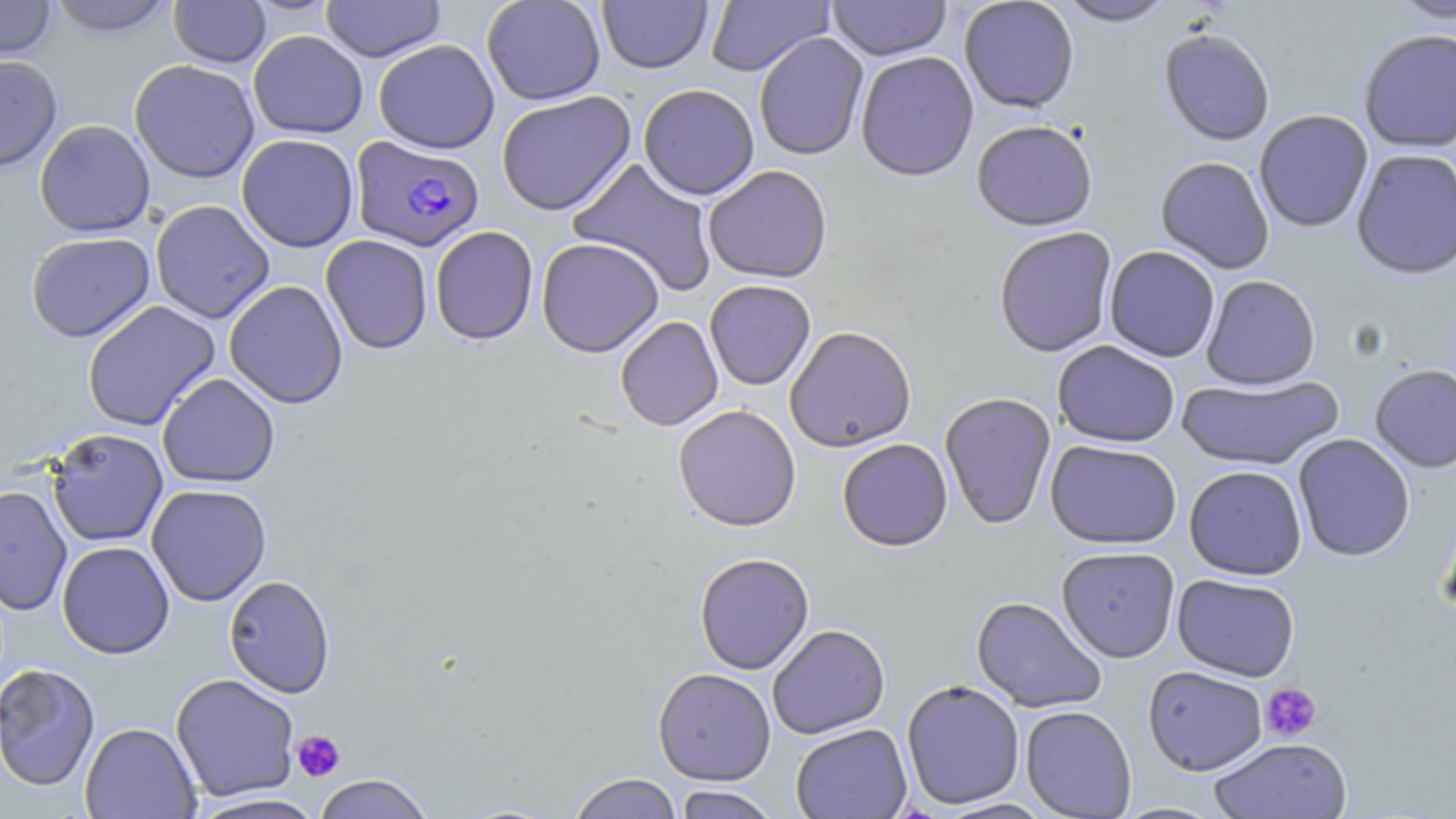
plasmodium_falciparum_infected_red_blood_cell_locations: 'approximate bounding boxes as named x1/y1/x2/y2 corners in pixels: (x1=350, y1=136, x2=485, y2=252)'
slide_level_diagnosis: Plasmodium falciparum
image_size: 1456×819 pixels
uninfected_red_blood_cell_locations: 'approximate bounding boxes as named x1/y1/x2/y2 corners in pixels: (x1=0, y1=0, x2=57, y2=61), (x1=45, y1=0, x2=177, y2=37), (x1=169, y1=0, x2=271, y2=68), (x1=321, y1=0, x2=446, y2=62), (x1=481, y1=0, x2=605, y2=105), (x1=705, y1=0, x2=833, y2=76), (x1=826, y1=0, x2=950, y2=61), (x1=959, y1=0, x2=1079, y2=113), (x1=1055, y1=0, x2=1177, y2=27), (x1=1388, y1=0, x2=1455, y2=26), (x1=597, y1=1, x2=712, y2=73), (x1=1158, y1=29, x2=1275, y2=147), (x1=248, y1=30, x2=368, y2=138), (x1=1359, y1=30, x2=1456, y2=154), (x1=753, y1=32, x2=868, y2=161), (x1=373, y1=38, x2=499, y2=154), (x1=855, y1=51, x2=979, y2=181), (x1=0, y1=55, x2=62, y2=172), (x1=129, y1=60, x2=260, y2=183), (x1=638, y1=83, x2=759, y2=200), (x1=496, y1=91, x2=636, y2=216), (x1=1255, y1=110, x2=1373, y2=233), (x1=34, y1=119, x2=156, y2=237), (x1=971, y1=120, x2=1098, y2=231), (x1=236, y1=134, x2=359, y2=252), (x1=1351, y1=149, x2=1456, y2=280), (x1=567, y1=157, x2=719, y2=297), (x1=1155, y1=157, x2=1274, y2=274), (x1=703, y1=165, x2=832, y2=283), (x1=150, y1=200, x2=275, y2=324), (x1=430, y1=226, x2=538, y2=345), (x1=993, y1=226, x2=1117, y2=357), (x1=26, y1=232, x2=155, y2=342), (x1=321, y1=235, x2=433, y2=354), (x1=536, y1=237, x2=664, y2=356), (x1=1104, y1=246, x2=1220, y2=362), (x1=1201, y1=275, x2=1321, y2=390), (x1=704, y1=279, x2=816, y2=390), (x1=224, y1=280, x2=348, y2=408), (x1=82, y1=300, x2=221, y2=431), (x1=615, y1=316, x2=723, y2=431), (x1=784, y1=326, x2=916, y2=452), (x1=1052, y1=341, x2=1180, y2=447), (x1=1370, y1=365, x2=1456, y2=473), (x1=157, y1=373, x2=280, y2=488), (x1=1177, y1=374, x2=1344, y2=471), (x1=939, y1=392, x2=1056, y2=530), (x1=673, y1=404, x2=801, y2=531), (x1=47, y1=428, x2=168, y2=547), (x1=1293, y1=434, x2=1415, y2=562), (x1=837, y1=438, x2=953, y2=551), (x1=1045, y1=440, x2=1182, y2=549), (x1=1184, y1=465, x2=1307, y2=580), (x1=146, y1=483, x2=272, y2=606), (x1=0, y1=485, x2=72, y2=615), (x1=57, y1=541, x2=175, y2=659), (x1=1056, y1=547, x2=1180, y2=662), (x1=694, y1=552, x2=814, y2=674), (x1=223, y1=574, x2=335, y2=698), (x1=1172, y1=574, x2=1300, y2=682), (x1=971, y1=595, x2=1107, y2=714), (x1=767, y1=624, x2=890, y2=739), (x1=1, y1=662, x2=101, y2=792), (x1=1143, y1=666, x2=1268, y2=775), (x1=653, y1=668, x2=776, y2=785), (x1=170, y1=672, x2=300, y2=801), (x1=901, y1=679, x2=1025, y2=809), (x1=1020, y1=705, x2=1136, y2=818), (x1=79, y1=722, x2=200, y2=819), (x1=790, y1=723, x2=912, y2=819), (x1=1209, y1=738, x2=1352, y2=818), (x1=567, y1=772, x2=683, y2=819), (x1=313, y1=773, x2=435, y2=819), (x1=672, y1=786, x2=782, y2=819), (x1=186, y1=793, x2=329, y2=819), (x1=936, y1=797, x2=1056, y2=818), (x1=1110, y1=801, x2=1227, y2=818)'
field_of_view: single
platelet_locations: 'approximate bounding boxes as named x1/y1/x2/y2 corners in pixels: (x1=1261, y1=682, x2=1322, y2=742), (x1=291, y1=730, x2=346, y2=781)'
modality: light microscopy
preparation: thin blood film
magnification: 1000x
stain: May-Grünwald-Giemsa